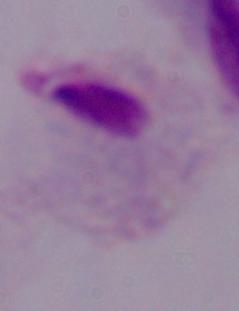

Summary:
  - Modality: micrograph
  - Magnification: 1000x
  - Identification: trichomonad